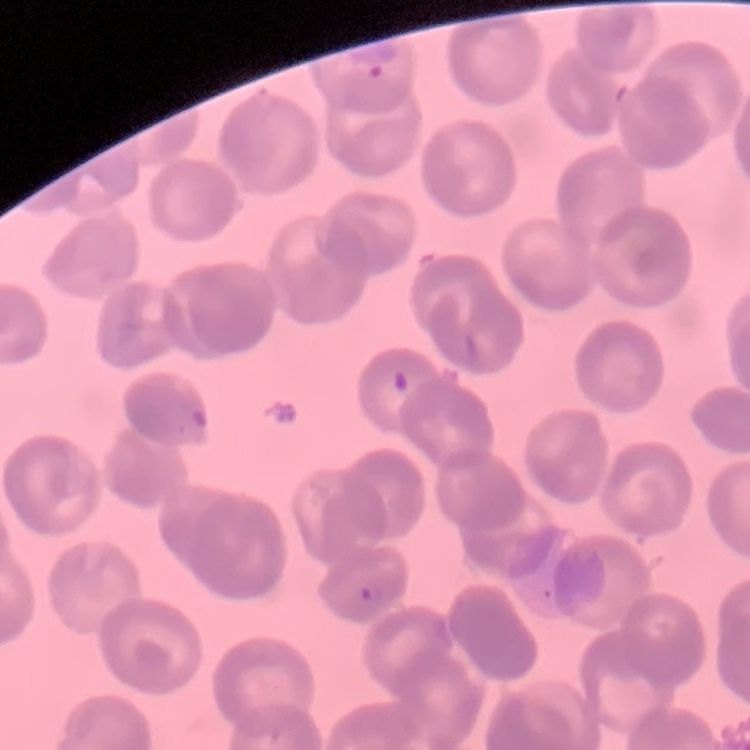

erythrocyte morphology = rouleaux formation
image type = one tile cut from a larger photomicrograph
stain = Field's or Giemsa
preparation = thin peripheral smear